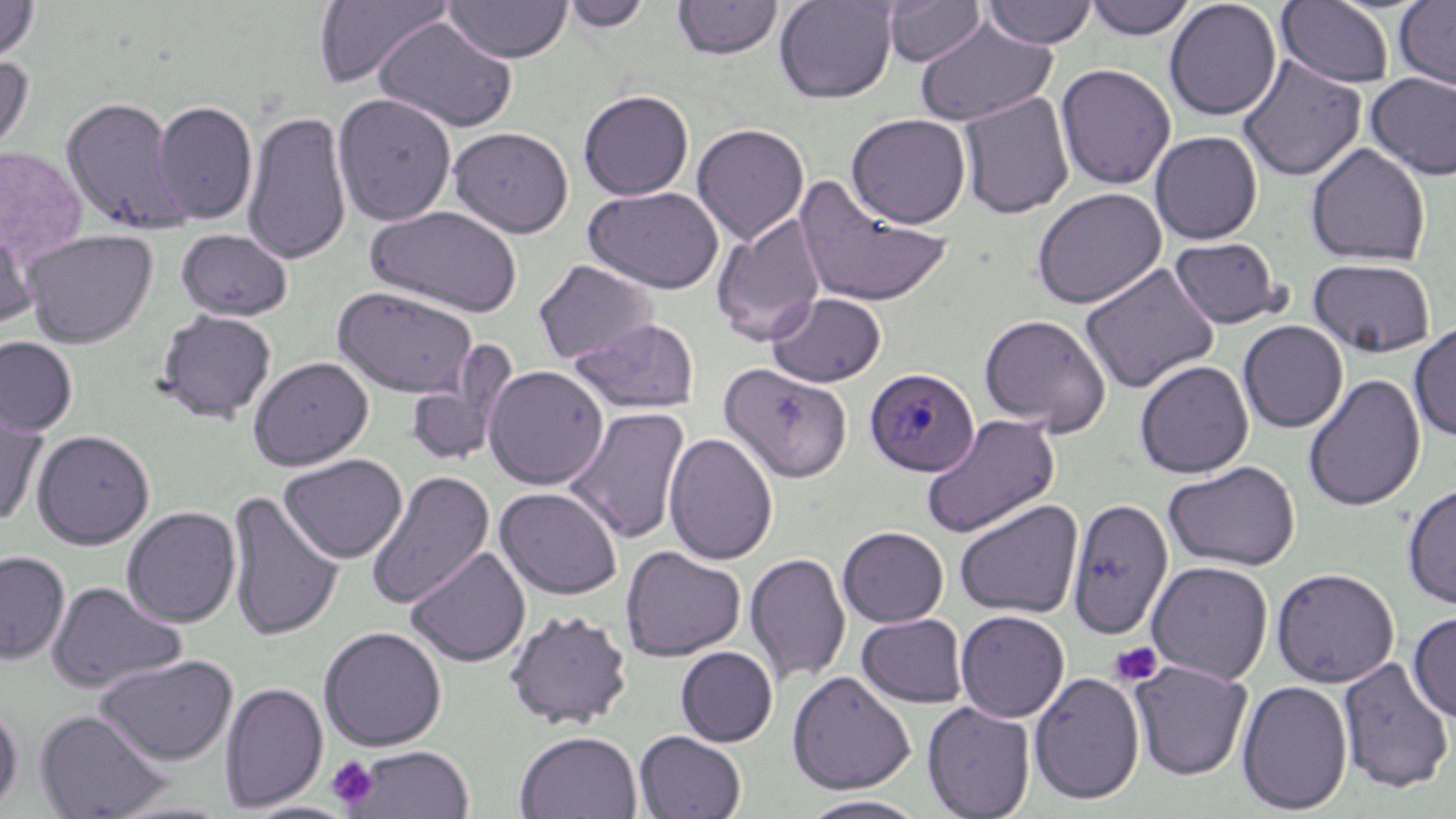
slide-level diagnosis = Plasmodium malariae
uninfected red blood cell locations = approximate bounding boxes as (x1, y1, x2, y2) in pixels: (0, 0, 40, 65), (774, 0, 899, 103), (1083, 0, 1199, 41), (1164, 0, 1282, 121), (312, 1, 456, 89), (443, 1, 572, 63), (560, 1, 654, 32), (671, 1, 785, 60), (882, 1, 989, 66), (981, 1, 1098, 49), (1393, 1, 1456, 90), (1276, 2, 1395, 88), (374, 16, 519, 132), (914, 17, 1058, 126), (0, 53, 35, 163), (1237, 54, 1367, 182), (1055, 63, 1177, 190), (1365, 71, 1456, 181), (578, 89, 694, 200), (957, 91, 1075, 219), (333, 92, 457, 226), (59, 96, 188, 235), (153, 99, 258, 225), (243, 109, 353, 266), (847, 113, 972, 228), (692, 123, 810, 245), (448, 126, 574, 237), (1150, 130, 1263, 244), (1305, 143, 1431, 266), (0, 144, 87, 270), (795, 175, 952, 308), (583, 186, 724, 294), (1031, 188, 1167, 309), (365, 204, 525, 317), (712, 213, 827, 344), (0, 224, 40, 334), (176, 228, 293, 320), (22, 229, 158, 347), (1169, 236, 1286, 328), (1308, 257, 1436, 357), (533, 259, 659, 366), (1079, 262, 1221, 394), (332, 285, 480, 397), (767, 291, 888, 386), (154, 309, 278, 423), (978, 313, 1112, 434), (570, 317, 700, 413), (1238, 320, 1348, 433), (1409, 320, 1456, 441), (0, 336, 79, 435), (402, 348, 517, 469), (248, 356, 374, 470), (1134, 359, 1254, 478), (718, 362, 852, 484), (483, 364, 610, 489), (1303, 374, 1426, 512), (0, 403, 49, 525), (564, 407, 691, 544), (921, 414, 1061, 539), (31, 429, 155, 549), (663, 431, 779, 565), (279, 453, 408, 562), (1164, 459, 1301, 570), (365, 469, 495, 610), (1401, 482, 1456, 609), (495, 486, 624, 599), (226, 490, 344, 642), (1066, 497, 1174, 640), (954, 499, 1083, 618), (121, 505, 241, 628), (837, 526, 949, 627), (621, 545, 746, 661), (406, 546, 531, 667), (0, 550, 70, 663), (745, 552, 851, 687), (1146, 560, 1273, 683), (1271, 567, 1400, 687), (46, 581, 187, 693), (504, 609, 633, 728), (955, 609, 1070, 722), (1408, 612, 1456, 721), (857, 613, 968, 708), (318, 626, 447, 751), (675, 646, 779, 746), (93, 653, 238, 764), (1337, 656, 1455, 793), (1130, 660, 1253, 780), (786, 671, 917, 794), (1029, 671, 1146, 804), (1236, 679, 1353, 815), (219, 681, 328, 812), (0, 700, 23, 815), (922, 701, 1036, 818), (33, 708, 173, 819), (514, 730, 643, 819), (635, 730, 747, 818), (344, 745, 477, 818), (799, 795, 930, 818), (104, 797, 239, 818), (240, 801, 360, 819)
stain = May-Grünwald-Giemsa
preparation = thin blood smear
platelet locations = approximate bounding boxes as (x1, y1, x2, y2) in pixels: (1108, 641, 1164, 688), (326, 756, 380, 810)
magnification = 1000x
modality = optical microscopy
field of view = one of a larger specimen
image size = 1456×819 pixels
Plasmodium malariae-infected red blood cell locations = approximate bounding boxes as (x1, y1, x2, y2) in pixels: (865, 367, 980, 476)